Classify this cell by malaria status.
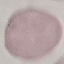
It is uninfected.

capture = smartphone through the microscope eyepiece
image type = automatically extracted cell patch, resized to 64 × 64 pixels
preparation = thin blood smear
stain = Giemsa